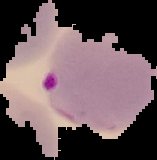

Result: malaria parasites detected. From a thin blood film. Image is 157×160 pixels. Segmented cell region on a black background.